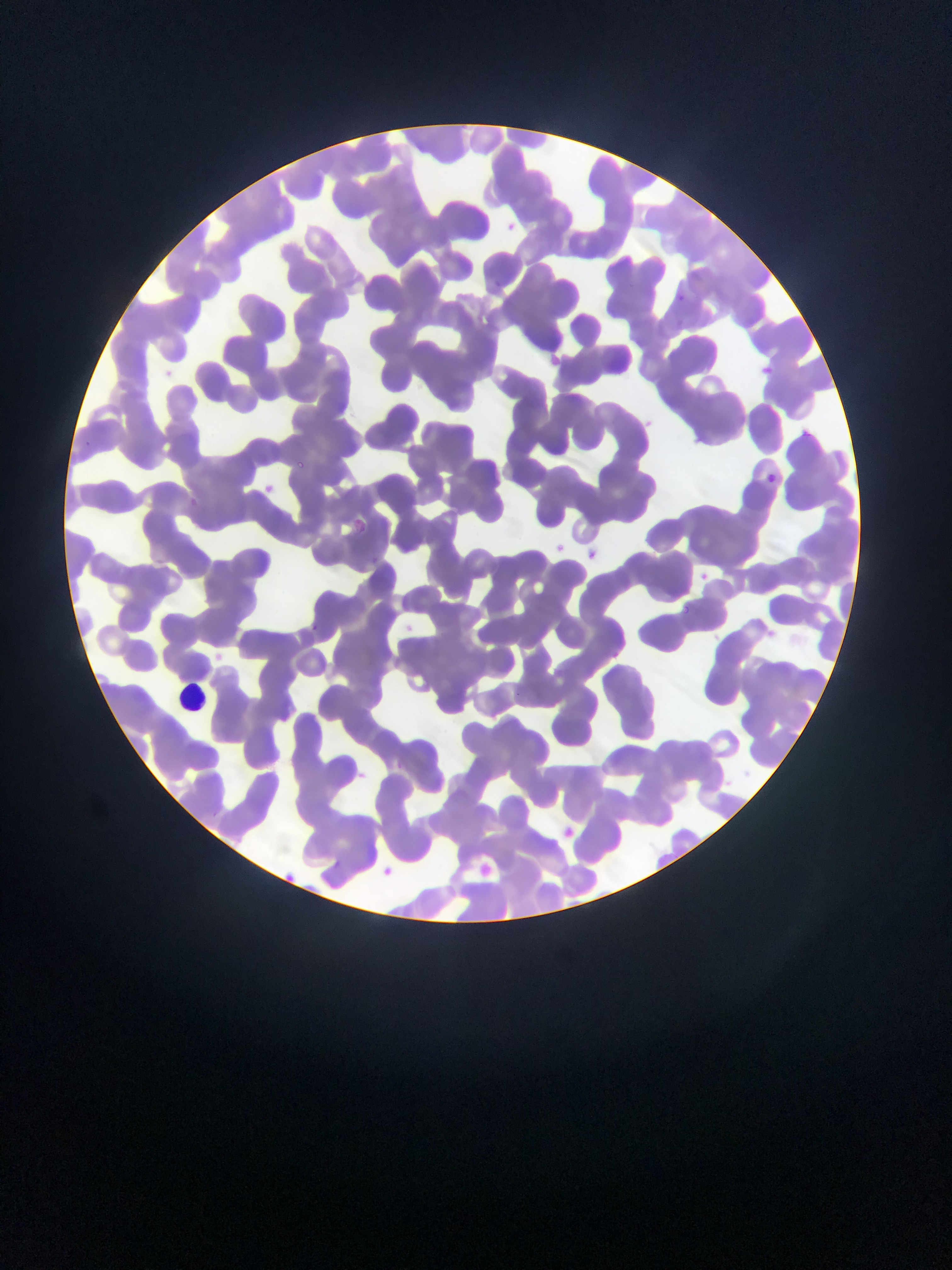
Approximate bounding boxes as left top right bottom in pixels.
Summary:
  - Plasmodium parasite locations: 492 278 504 292; 679 292 685 302; 295 461 311 472; 765 473 775 483; 353 520 364 535; 680 603 691 615; 310 624 317 632
  - Leukocyte locations: 176 683 207 712
  - Country: Ghana
  - Preparation: thin blood film
  - Capture: mobile-phone photograph through a microscope
  - Image size: 952×1270 pixels
  - Field of view: single